Assess this cell for malaria.
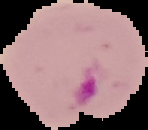

It is parasitized.

The area outside the segmented cell region is set to black. Image is 148×130 pixels. From a thin blood smear.